State which parasite is depicted.
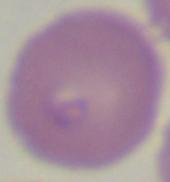
This is Babesia.

1000x magnification. Micrograph.